Name the parasite shown.
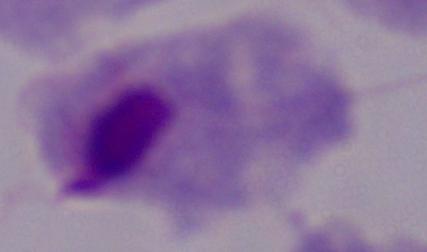

This is a trichomonad.

Captured at 1000x magnification. Micrograph.